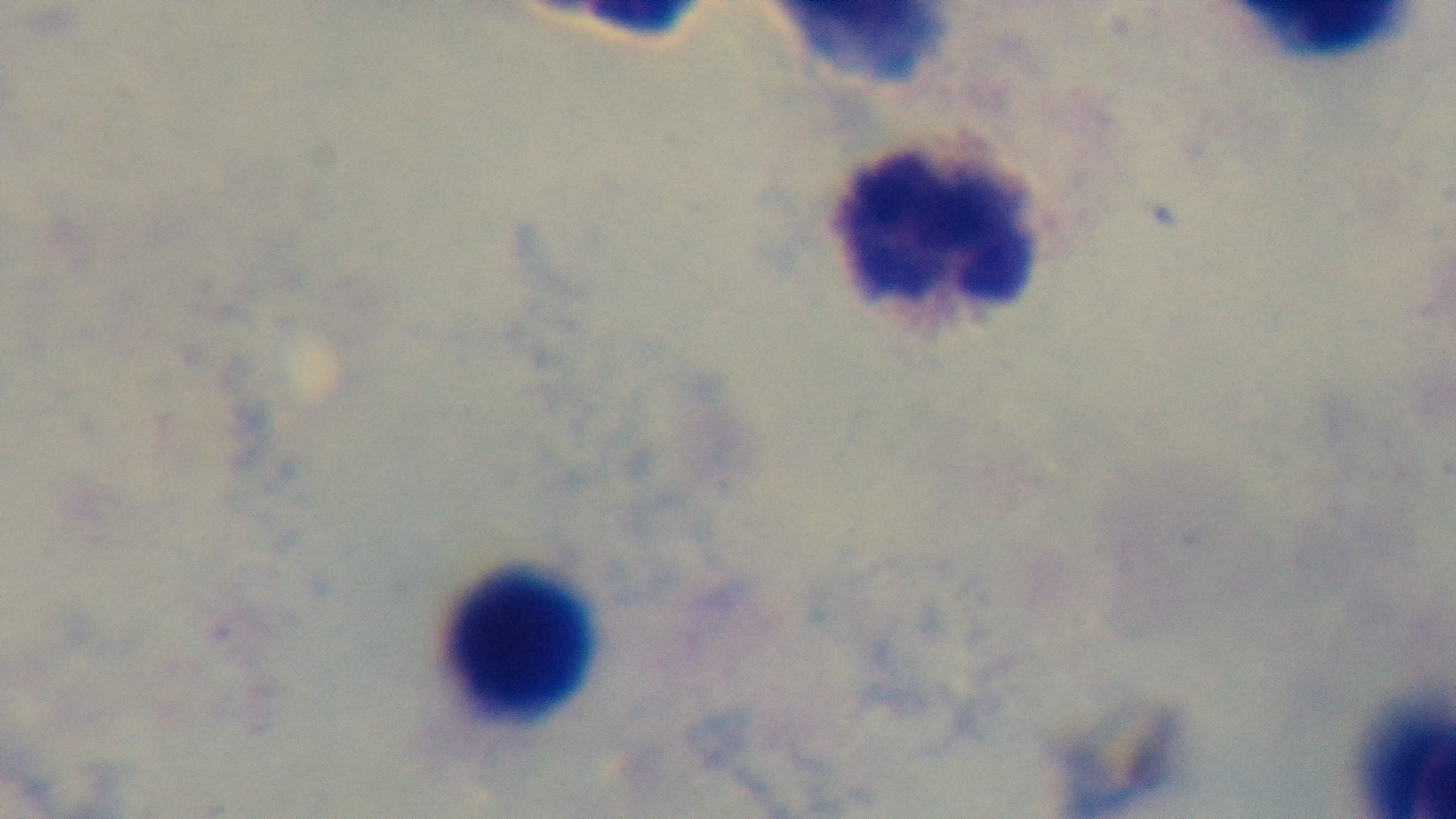 Malaria status: uninfected. Single field of view. Photomicrograph. 100x oil-immersion objective. Preparation: thick blood film. Giemsa-stained. Captured with a mounted 4K digital camera.